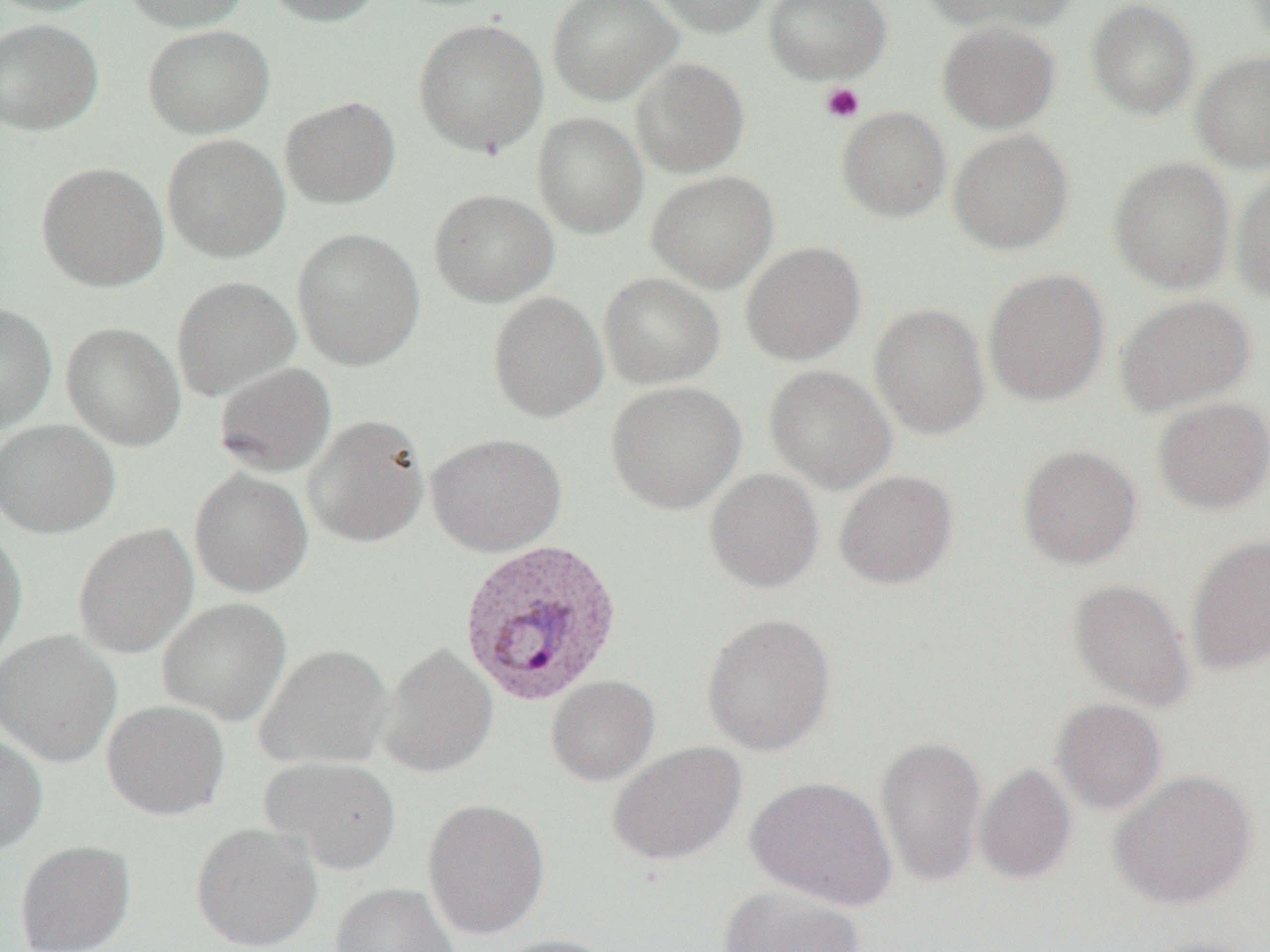 Approximate bounding boxes as (x1,y1)-(x2,y2) corner pairs in pixels. Plasmodium vivax-infected red blood cell locations: (458,537)-(624,706). Uninfected red blood cell locations: (0,0)-(112,17), (120,0)-(250,33), (263,0)-(384,26), (547,0)-(682,105), (644,0)-(772,37), (763,0)-(891,84), (925,0)-(1077,33), (1086,0)-(1200,119), (413,18)-(548,158), (0,19)-(102,135), (937,20)-(1060,133), (143,24)-(275,138), (1191,50)-(1270,172), (630,57)-(750,178), (280,95)-(400,208), (836,106)-(951,222), (532,112)-(648,238), (948,129)-(1074,255), (162,133)-(290,263), (1107,156)-(1235,294), (36,161)-(169,292), (1231,168)-(1270,303), (647,170)-(779,293), (429,189)-(559,307), (292,227)-(425,370), (741,241)-(866,365), (982,268)-(1110,406), (598,272)-(725,389), (172,276)-(300,401), (488,291)-(608,423), (1114,293)-(1255,416), (869,302)-(991,440), (0,303)-(57,434), (61,322)-(185,450), (214,361)-(337,477), (764,365)-(896,494), (606,381)-(746,515), (1153,396)-(1270,515), (304,413)-(431,548), (0,419)-(120,538), (426,432)-(567,557), (1017,443)-(1142,569), (189,468)-(313,597), (704,468)-(824,593), (835,469)-(958,589), (73,523)-(198,658), (0,529)-(27,662), (1186,534)-(1270,675), (1067,578)-(1195,712), (157,597)-(291,726), (701,613)-(836,756), (0,629)-(122,767), (377,641)-(498,779), (254,643)-(394,770), (546,675)-(660,787), (1051,698)-(1167,815), (102,699)-(230,820), (0,732)-(47,856), (875,734)-(987,887), (607,742)-(747,866), (261,756)-(400,875), (974,763)-(1077,885), (1109,769)-(1257,910), (745,775)-(898,911), (422,798)-(551,941), (190,821)-(323,951), (14,840)-(135,952), (331,883)-(460,952), (718,885)-(865,952), (491,934)-(618,952), (1144,935)-(1264,952). Platelet locations: (819,82)-(864,123). Slide-level diagnosis: Plasmodium vivax. One field of a larger specimen. Light microscopy. Thin blood film. Image is 1270×952 pixels. Captured at 1000x magnification.